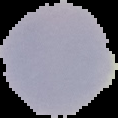 Image is 118×118 pixels. From a thin blood film. The area outside the segmented cell region is set to black. Result: negative for Plasmodium parasites.